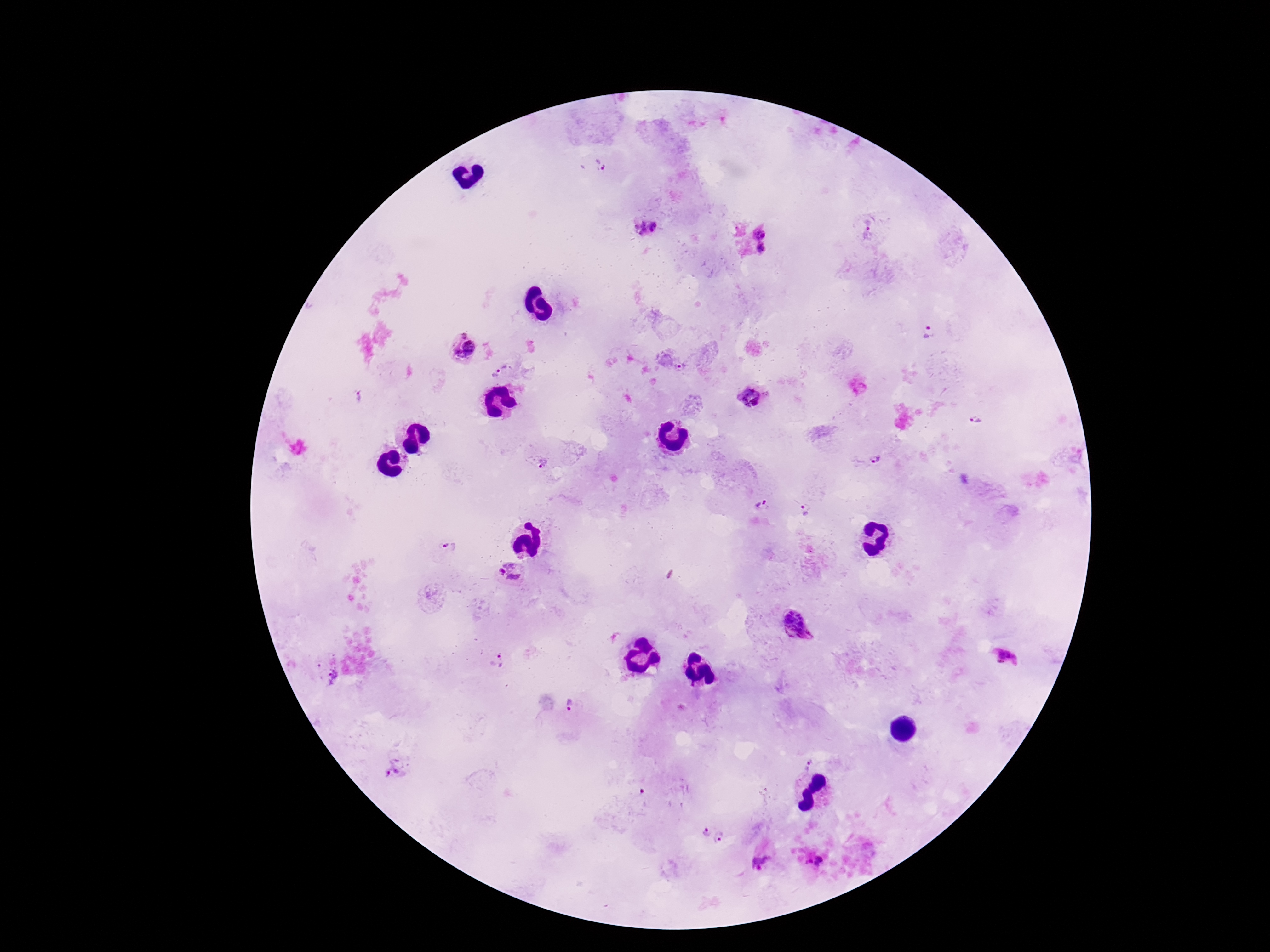
image size = 1270×952 pixels
capture = smartphone camera through the microscope eyepiece
stain = Giemsa
Plasmodium parasite locations = approximate centers as [x, y] in pixels: [599, 165], [869, 225], [645, 226], [638, 227], [654, 227], [642, 233], [761, 233], [761, 248], [928, 332], [463, 337], [471, 349], [457, 353], [680, 366], [500, 370], [766, 394], [749, 396], [360, 397], [976, 420], [875, 460], [542, 464], [762, 506], [802, 512], [450, 546], [511, 564], [502, 572], [513, 578], [799, 624], [1007, 657], [503, 660], [333, 677], [570, 707], [809, 763], [394, 768], [707, 832], [720, 837], [819, 859], [760, 862]
patient malaria status = infected
field of view = single
magnification = 100x
preparation = thick blood smear